Assess this cell for malaria.
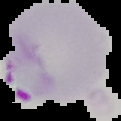
Parasitized.

Summary:
  - Image size: 121×121 pixels
  - Preparation: thin blood film
  - Image type: segmented cell region on a black background